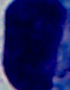

Summary:
  - Modality: photomicrograph
  - Identification: leukocyte
  - Magnification: 1000x